Identify the blood parasite species.
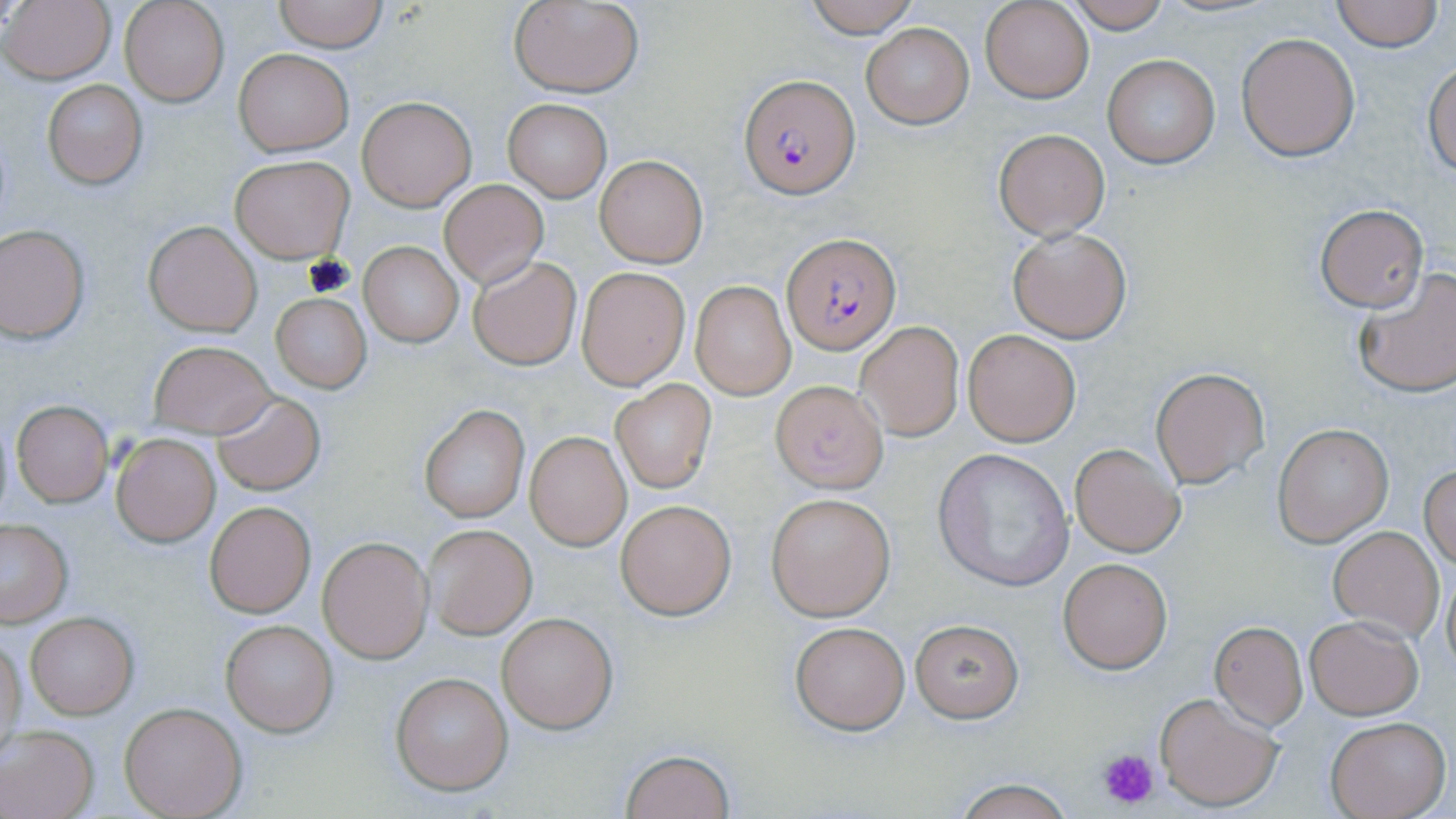

Plasmodium falciparum.

Approximate bounding boxes as (x1,y1)-(x2,y2) corner pairs in pixels. Platelet locations: (1097,746)-(1159,809). Uninfected red blood cell locations: (2,0)-(116,85), (120,0)-(228,107), (274,0)-(386,52), (803,0)-(921,37), (980,0)-(1093,103), (1064,0)-(1172,32), (1331,0)-(1442,51), (508,1)-(645,96), (861,23)-(973,129), (1237,34)-(1360,160), (234,49)-(352,155), (1101,55)-(1220,169), (1424,61)-(1456,177), (43,79)-(147,190), (357,96)-(476,210), (504,99)-(611,201), (992,128)-(1110,241), (231,155)-(353,262), (594,156)-(706,267), (440,180)-(548,288), (1313,203)-(1430,312), (144,220)-(262,336), (1,226)-(92,342), (1008,227)-(1131,344), (360,241)-(463,346), (468,255)-(583,371), (575,266)-(690,391), (1352,268)-(1456,399), (691,281)-(795,400), (271,293)-(371,393), (854,321)-(964,441), (963,330)-(1080,446), (148,341)-(273,438), (1150,367)-(1270,489), (771,380)-(889,491), (612,382)-(716,494), (213,392)-(325,495), (11,401)-(113,506), (419,405)-(530,522), (1273,424)-(1392,545), (111,431)-(221,546), (525,432)-(632,550), (1070,443)-(1186,559), (933,448)-(1075,592), (1420,466)-(1456,569), (766,492)-(895,621), (615,498)-(736,620), (204,500)-(315,618), (0,520)-(73,626), (424,525)-(535,639), (1329,526)-(1443,638), (318,537)-(431,662), (1059,557)-(1172,673), (1443,568)-(1456,676), (496,610)-(619,733), (25,612)-(138,719), (1305,616)-(1423,719), (221,619)-(337,736), (788,619)-(910,735), (910,619)-(1023,722), (1209,621)-(1308,729), (1,636)-(25,755), (389,672)-(513,795), (1155,693)-(1283,813), (121,701)-(245,819), (1325,716)-(1450,819), (0,727)-(99,819), (620,748)-(735,819), (947,776)-(1077,818). Plasmodium falciparum-infected red blood cell locations: (738,73)-(859,198), (784,234)-(900,352). Optical microscopy. Thin blood smear. One field of a larger specimen. Captured at 1000x magnification. Image is 1456×819 pixels. May-Grünwald-Giemsa stain.